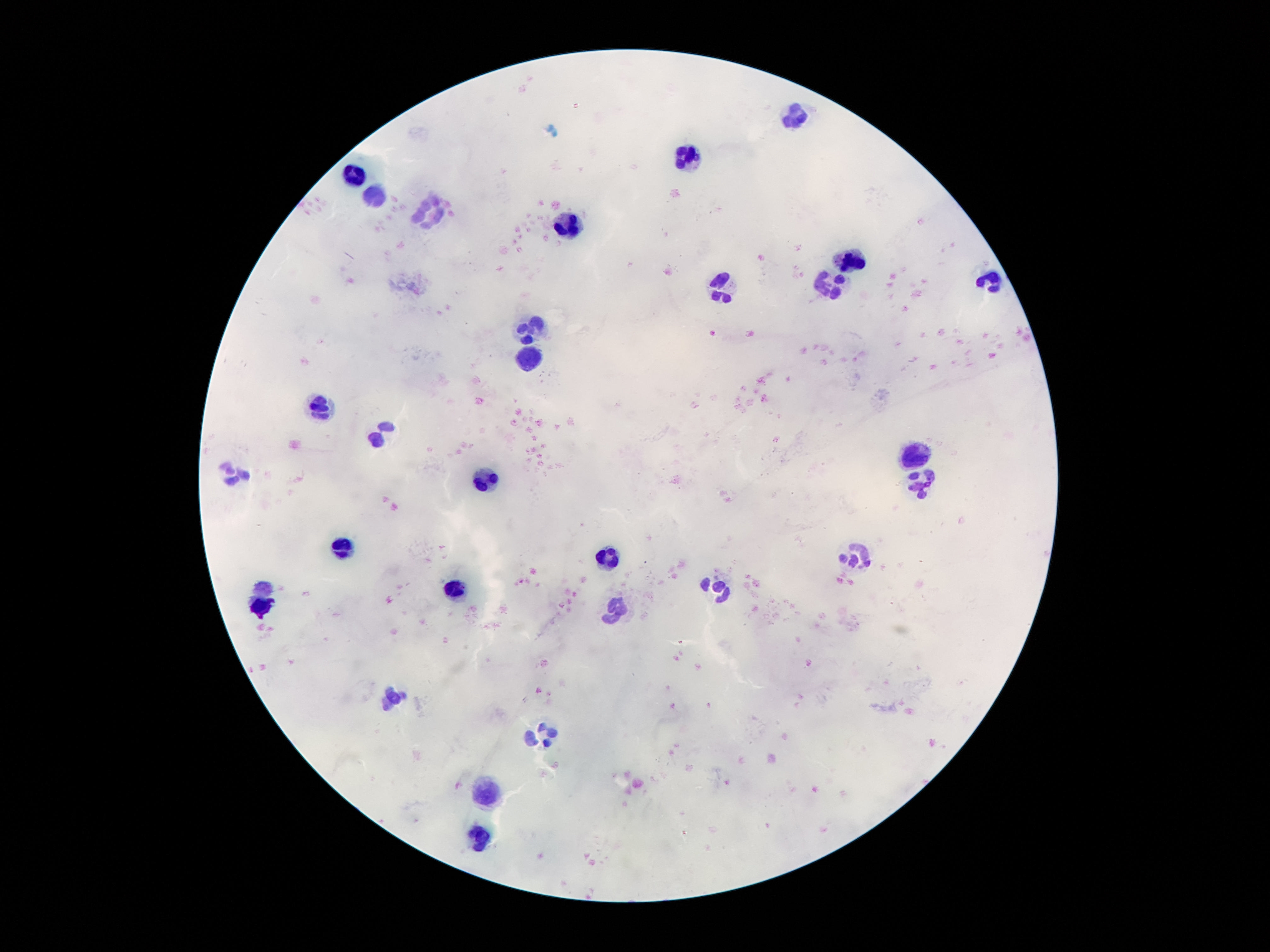
image size = 1270×952 pixels
leukocyte locations = approximate centers as [x, y] in pixels: [794, 117], [688, 159], [355, 176], [378, 197], [429, 212], [567, 223], [854, 262], [990, 279], [831, 281], [721, 288], [530, 330], [528, 363], [318, 401], [383, 434], [913, 452], [233, 473], [485, 477], [922, 484], [343, 551], [857, 556], [607, 561], [262, 587], [719, 588], [457, 589], [259, 607], [616, 609], [390, 697], [542, 735], [488, 792], [481, 838]
patient malaria status = negative
capture = smartphone camera through the microscope eyepiece
preparation = thick peripheral-blood smear
stain = Giemsa
magnification = 100x
field of view = one from this slide